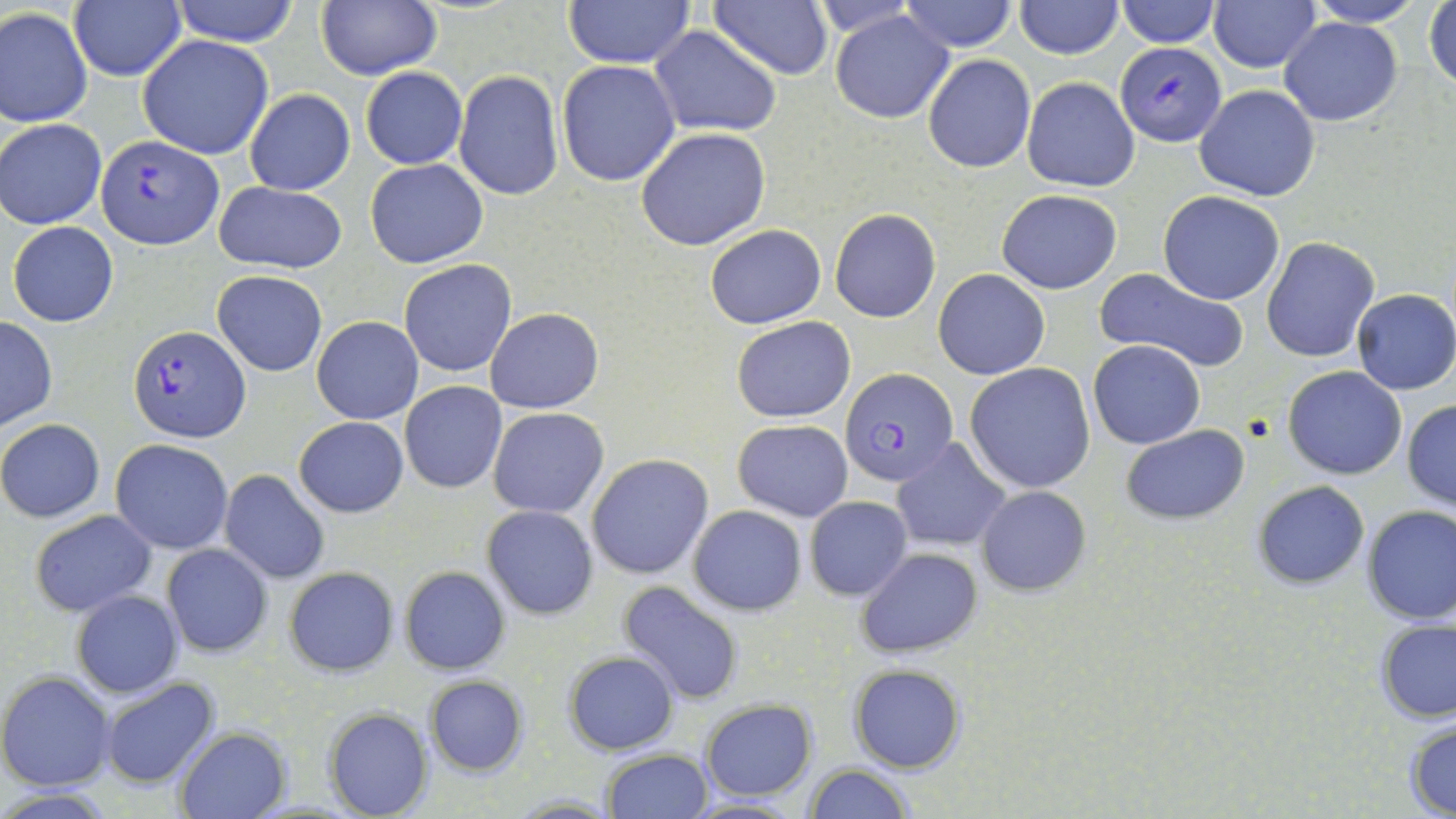 Approximate bounding boxes as (x1, y1, x2, y2) in pixels. Uninfected red blood cell locations: (170, 0, 301, 45), (316, 0, 439, 81), (562, 0, 696, 69), (900, 0, 1018, 52), (1014, 0, 1124, 58), (1116, 0, 1219, 47), (1304, 0, 1425, 27), (709, 1, 833, 80), (1208, 1, 1321, 74), (1426, 1, 1456, 95), (69, 2, 186, 82), (803, 2, 927, 36), (0, 7, 92, 127), (831, 9, 955, 123), (1279, 17, 1401, 126), (650, 26, 782, 136), (138, 35, 276, 160), (923, 53, 1035, 172), (556, 60, 681, 186), (360, 68, 467, 169), (453, 69, 564, 201), (1022, 78, 1141, 191), (1195, 84, 1320, 201), (245, 89, 355, 196), (1, 118, 106, 229), (635, 127, 771, 250), (366, 158, 489, 267), (213, 180, 347, 274), (996, 189, 1123, 294), (1158, 190, 1285, 306), (828, 209, 941, 323), (8, 221, 120, 327), (704, 224, 827, 330), (1261, 236, 1380, 361), (399, 258, 517, 378), (933, 269, 1050, 379), (1097, 269, 1250, 374), (212, 271, 326, 376), (1352, 289, 1456, 395), (485, 308, 603, 414), (0, 315, 57, 431), (312, 316, 423, 424), (732, 317, 855, 421), (1089, 340, 1205, 449), (964, 363, 1096, 492), (1282, 366, 1407, 480), (400, 382, 508, 493), (1403, 399, 1456, 510), (488, 407, 609, 518), (295, 416, 408, 517), (1, 418, 105, 522), (733, 419, 852, 522), (1122, 426, 1249, 525), (527, 432, 669, 573), (890, 437, 1011, 554), (112, 440, 234, 553), (585, 453, 713, 579), (219, 470, 331, 584), (1251, 480, 1370, 590), (976, 486, 1091, 596), (805, 496, 913, 600), (482, 504, 599, 620), (1360, 504, 1456, 625), (688, 505, 806, 615), (31, 510, 157, 616), (161, 544, 272, 657), (855, 546, 982, 659), (283, 566, 399, 676), (399, 566, 511, 675), (618, 581, 743, 706), (71, 590, 184, 697), (1375, 617, 1456, 723), (564, 650, 679, 755), (848, 664, 965, 773), (0, 672, 117, 790), (423, 675, 531, 777), (99, 678, 221, 788), (699, 699, 817, 800), (324, 709, 433, 819), (1404, 718, 1456, 817), (175, 727, 290, 818), (600, 748, 713, 819), (802, 763, 914, 819), (0, 789, 121, 819), (678, 797, 807, 818). Plasmodium falciparum-infected red blood cell locations: (1119, 43, 1226, 146), (96, 136, 221, 248), (129, 325, 250, 443), (843, 369, 957, 488). Slide-level diagnosis: Plasmodium falciparum. Optical microscopy. Thin blood film. Image is 1456×819 pixels. May-Grünwald-Giemsa-stained preparation. Single field of view. 1000x magnification.